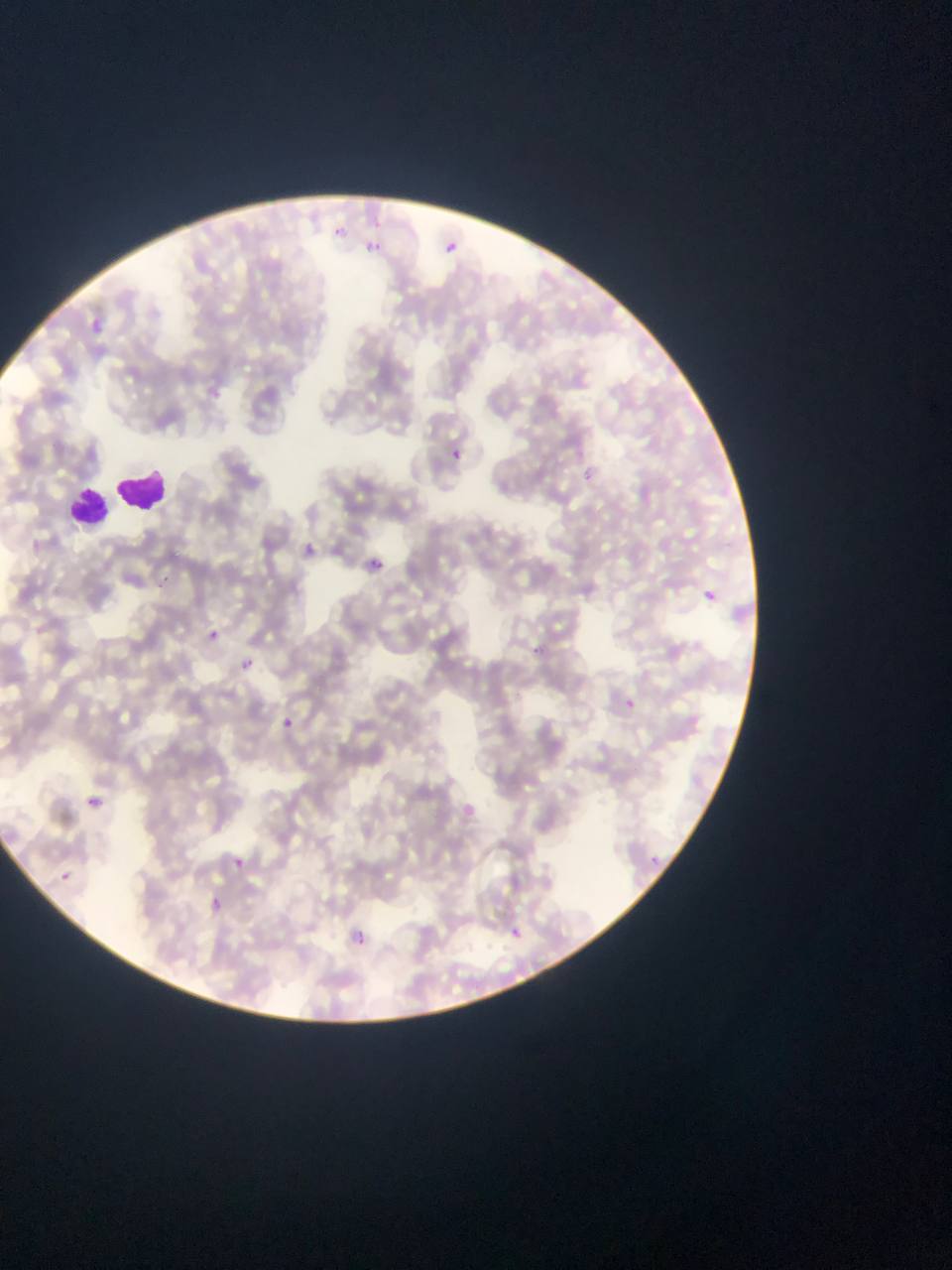
preparation = thin blood smear
field of view = single
image size = 952×1270 pixels
country = Ghana
capture = mobile-phone photograph through a microscope
leukocyte locations = approximate bounding boxes as [left, top, right, bottom] in pixels: [114, 464, 170, 516], [74, 474, 148, 529], [64, 479, 116, 532]
malaria parasite locations = approximate bounding boxes as [left, top, right, bottom] in pixels: [338, 227, 348, 237], [443, 236, 463, 253], [372, 238, 389, 259], [82, 312, 101, 337], [445, 445, 466, 465], [583, 468, 594, 482], [298, 540, 318, 560], [368, 557, 382, 570], [161, 570, 172, 577], [698, 588, 720, 606], [205, 628, 220, 643], [529, 643, 546, 654], [236, 656, 253, 672], [626, 697, 636, 708], [272, 711, 302, 738], [84, 794, 104, 812], [225, 849, 254, 874], [650, 851, 670, 870], [56, 868, 75, 886], [202, 894, 227, 917], [500, 920, 527, 947], [343, 924, 377, 953]